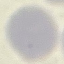
Summary:
  - Malaria status: uninfected
  - Capture: smartphone through the microscope eyepiece
  - Preparation: thin blood film
  - Image type: automatically extracted cell patch, resized to 64 × 64 pixels
  - Stain: Giemsa